Identify the parasite.
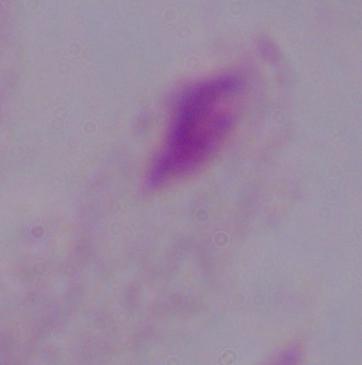

A trichomonad.

1000x magnification. Photomicrograph.